Name the parasite shown.
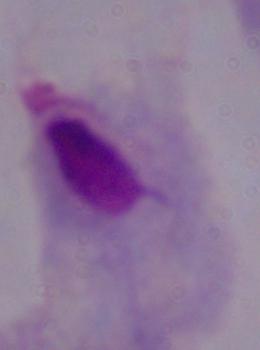

A trichomonad.

{
  "magnification": "1000x",
  "modality": "photomicrograph"
}